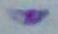
identification = Toxoplasma gondii
modality = photomicrograph
magnification = 1000x